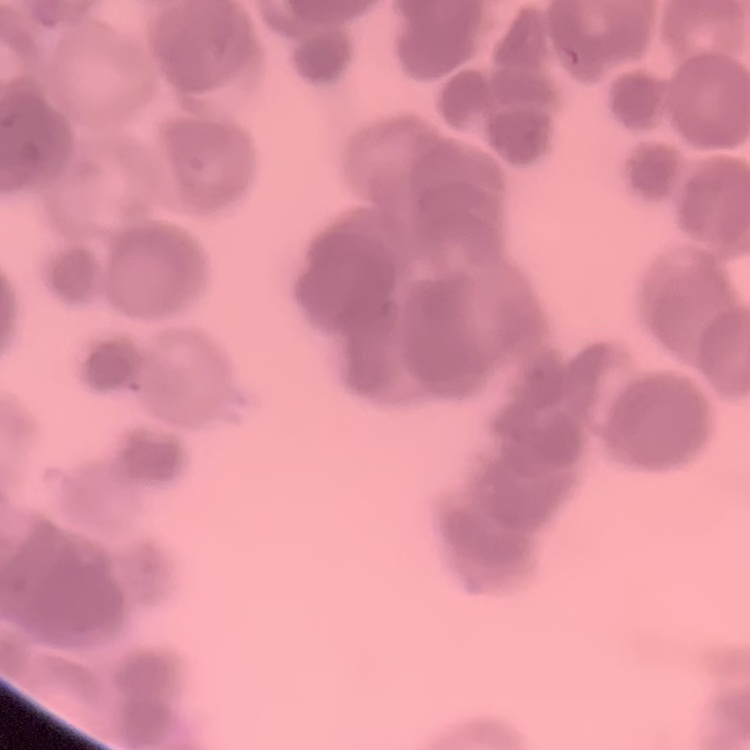 The erythrocytes show rouleaux formation. Thin blood smear. Stained with either Field's or Giemsa. Square crop of a larger photomicrograph.